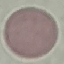

Summary:
  - Malaria status: uninfected
  - Preparation: thin blood smear
  - Stain: Giemsa
  - Image type: automatically extracted cell patch, resized to 64 × 64 pixels
  - Capture: smartphone camera at the microscope eyepiece